Classify this cell by malaria status.
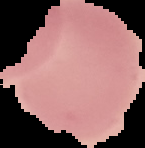

It is uninfected.

From a thin blood smear. Image is 145×148 pixels. Cell region segmented out of the field of view; the surrounding area is masked to black.